State which parasite is depicted.
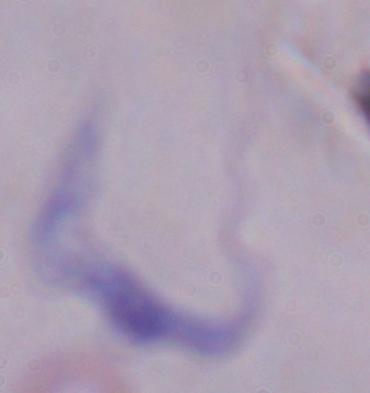
A trypanosome.

Summary:
  - Modality: micrograph
  - Magnification: 1000x